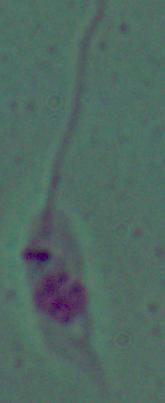

magnification = 1000x
modality = photomicrograph
identification = Leishmania